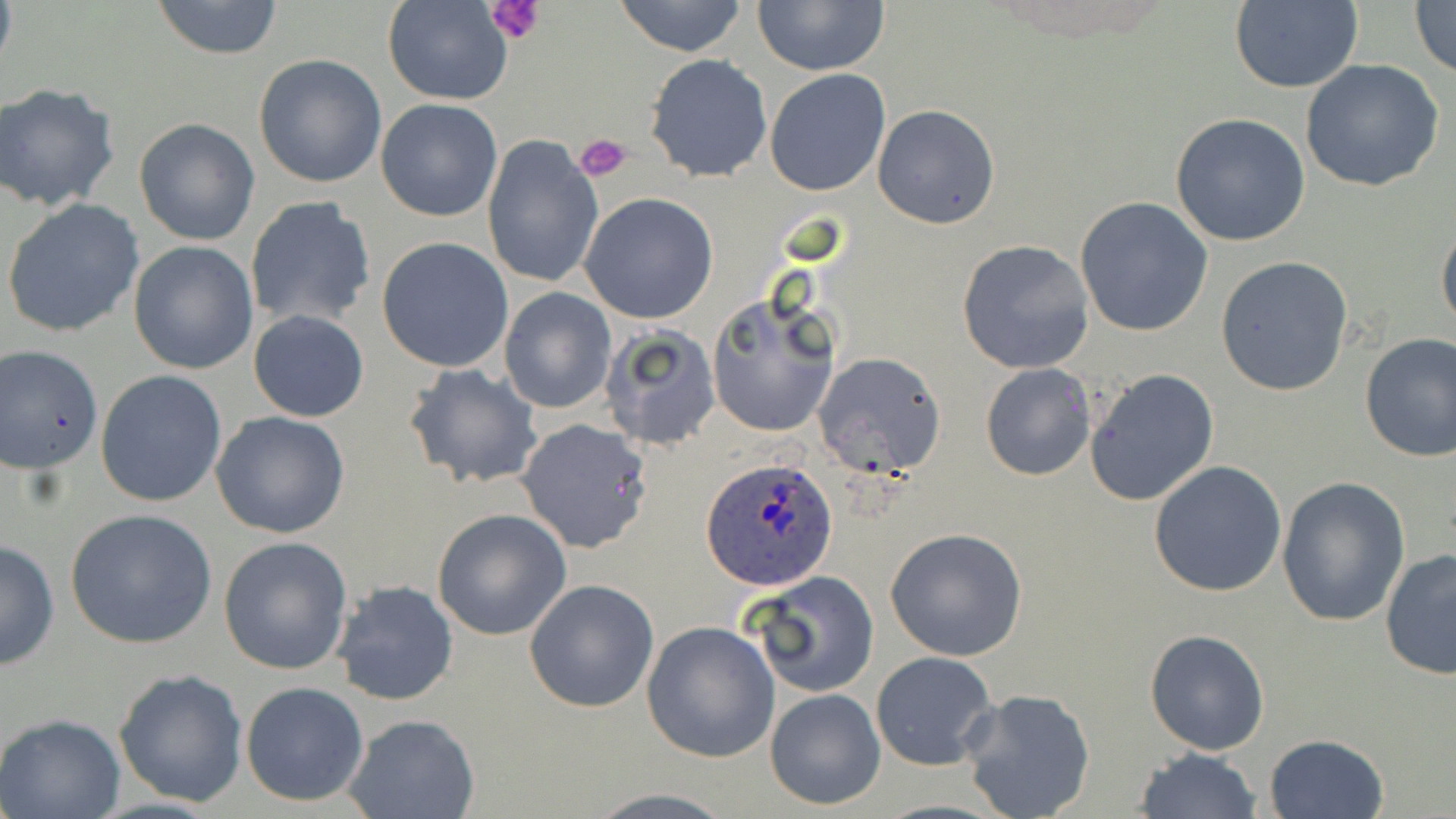
Approximate bounding boxes as (x1,y1)-(x2,y2) corner pairs in pixels. Plasmodium ovale-infected red blood cell locations: (704,459)-(838,589). Uninfected red blood cell locations: (149,0)-(285,59), (610,0)-(751,58), (384,1)-(513,105), (1410,1)-(1456,81), (752,2)-(890,76), (1227,2)-(1364,93), (253,53)-(388,188), (644,54)-(772,182), (1299,59)-(1444,193), (764,69)-(890,194), (0,84)-(122,212), (376,99)-(503,221), (873,104)-(1000,229), (1169,113)-(1313,248), (133,118)-(260,246), (482,134)-(604,291), (579,192)-(719,323), (1075,196)-(1213,338), (245,197)-(375,331), (3,198)-(146,338), (1436,212)-(1456,342), (377,237)-(513,373), (957,239)-(1094,375), (127,240)-(258,375), (1215,255)-(1354,396), (499,289)-(615,412), (705,292)-(840,438), (248,309)-(369,422), (600,324)-(721,451), (1357,332)-(1456,461), (0,346)-(104,471), (812,352)-(949,480), (980,362)-(1098,481), (404,363)-(543,490), (1086,367)-(1221,506), (95,370)-(227,507), (212,411)-(350,538), (516,420)-(654,555), (1147,460)-(1287,598), (1275,476)-(1410,627), (65,509)-(219,650), (432,509)-(572,641), (884,527)-(1029,663), (218,535)-(353,675), (1,536)-(58,672), (1380,549)-(1456,680), (744,570)-(879,698), (524,578)-(659,713), (331,579)-(458,708), (641,620)-(781,762), (1146,630)-(1269,755), (871,651)-(998,770), (114,667)-(250,806), (240,681)-(369,806), (960,686)-(1098,819), (765,689)-(885,809), (0,713)-(126,819), (342,714)-(480,819), (1264,734)-(1388,818), (1132,748)-(1262,819), (584,789)-(740,819). Platelet locations: (484,0)-(546,43), (575,131)-(631,183). Slide-level diagnosis: Plasmodium ovale. Thin blood film. Light microscopy. Captured at 1000x magnification. Single field of view. Image is 1456×819 pixels. May-Grünwald-Giemsa-stained preparation.